Report the malaria status of this cell.
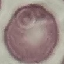
Uninfected.

Acquired by smartphone through the microscope eyepiece. Giemsa stain. Thin smear of blood. Cell patch, automatically extracted from a larger field of view and resized to 64 × 64 pixels.